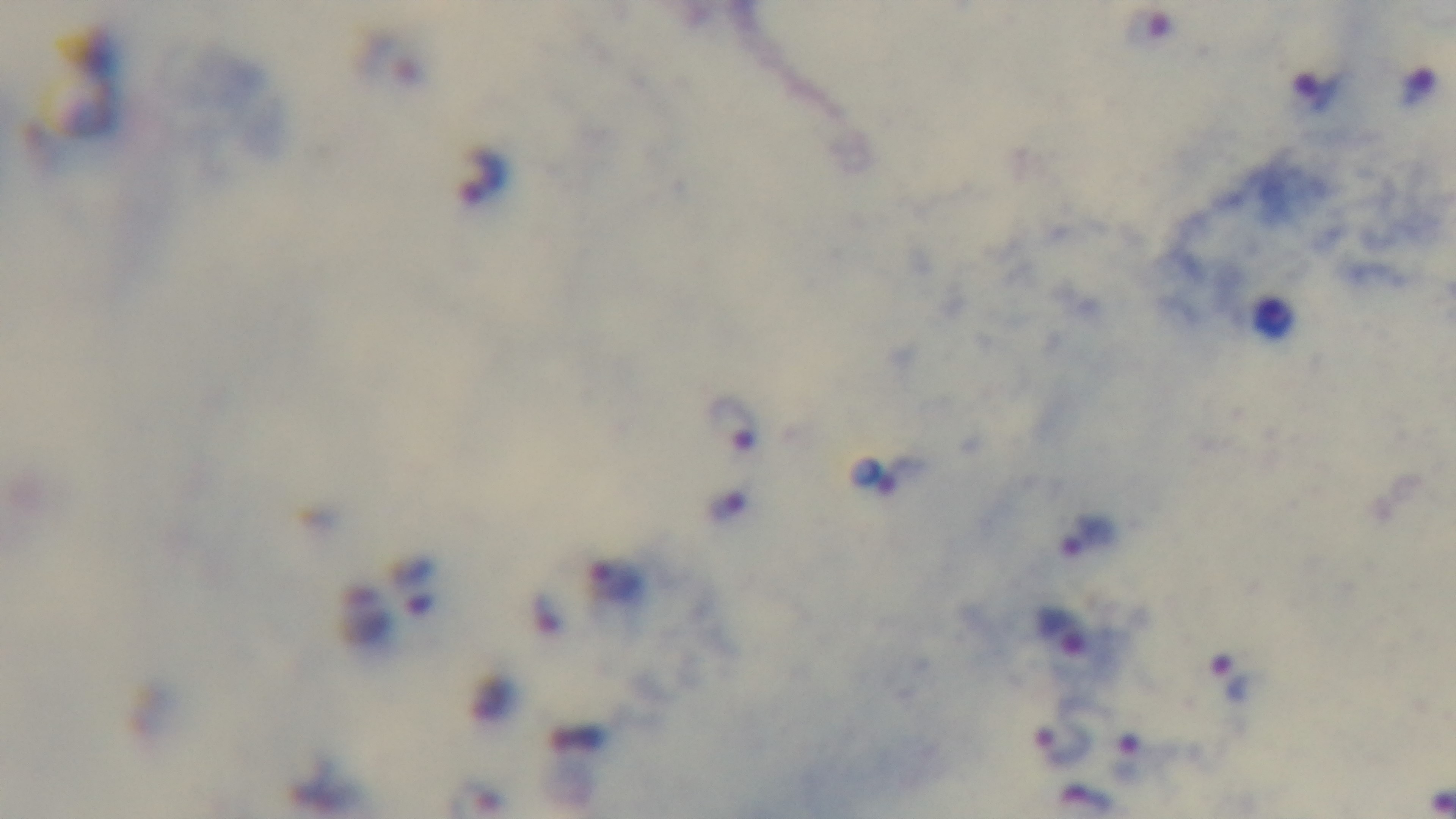

Summary:
  - Field of view: one from the slide
  - Preparation: thick blood film
  - Malaria status: infected
  - Objective: 100x oil immersion
  - Modality: light microscopy
  - Capture: mounted 4K digital camera
  - Stain: Giemsa